Name the cell type shown.
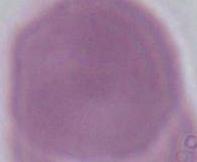
This is an erythrocyte.

{
  "magnification": "1000x",
  "modality": "photomicrograph"
}